Give a bounding box for every parasitised red blood cell, every trophozoite, every gametocyte, every leukocyte, and every artifact (platelet-like body, stain precipitate, or debris).
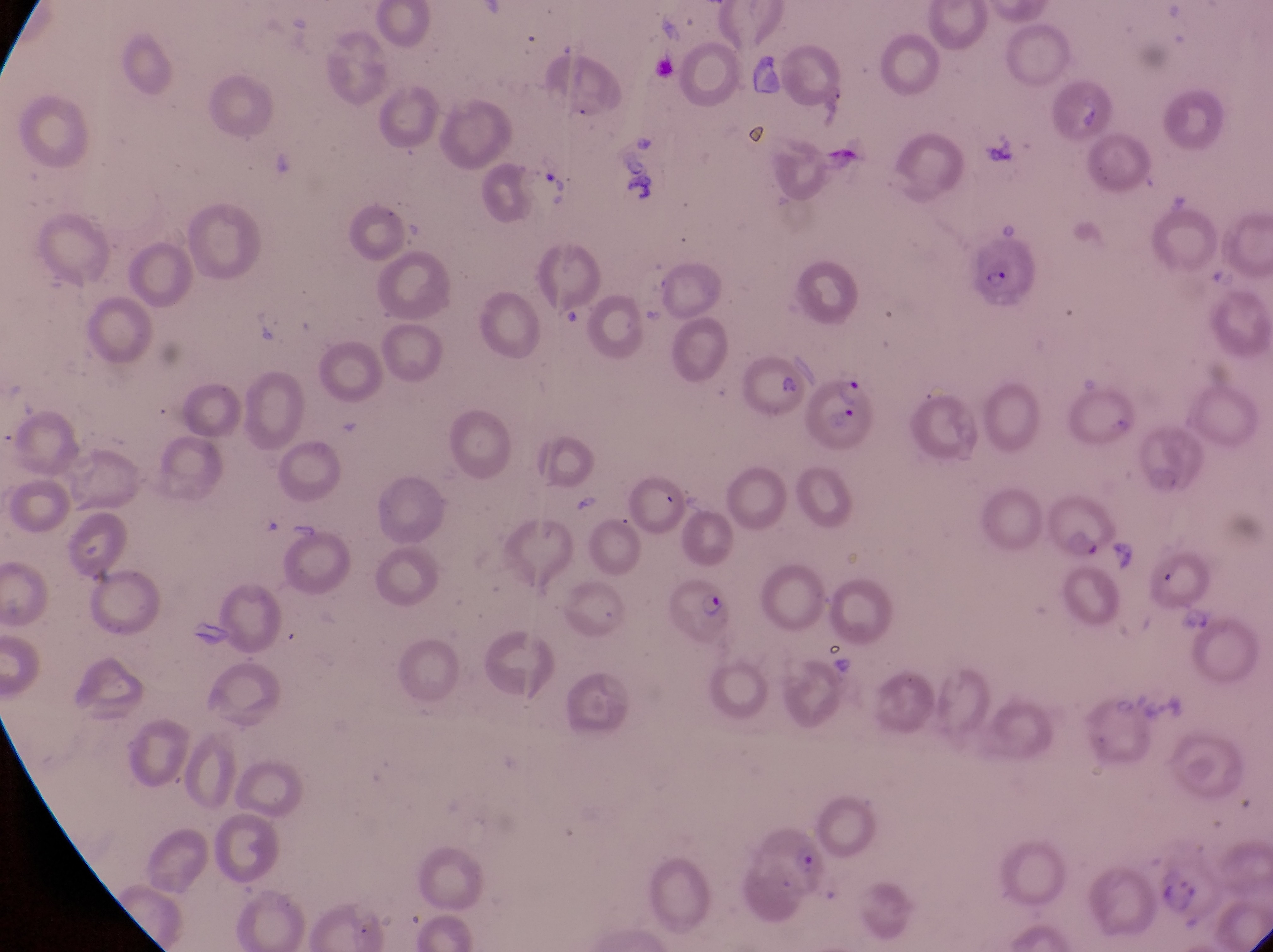

Approximate bounding boxes as left top right bottom in pixels.
Parasitised red blood cells: 963 235 1050 313; 799 365 876 450; 1043 491 1121 563; 662 580 742 642.
No leukocytes observed.

Thin blood smear. Photographed through the eyepiece of an Olympus CX-23 microscope with a smartphone camera. Sample from Uganda. Image is 1273×952 pixels. Magnification of 1000x. Single field of view.